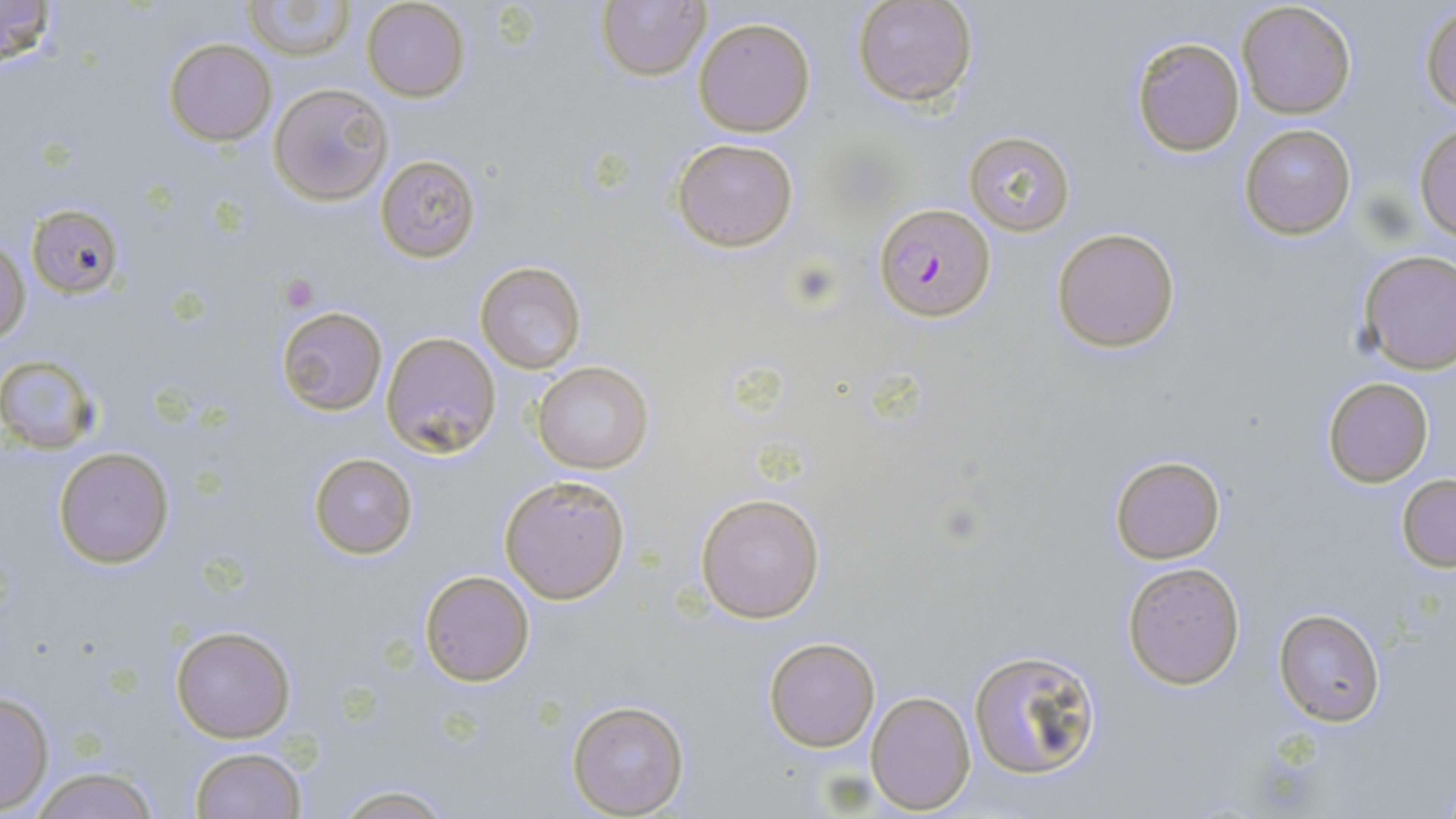
slide-level diagnosis = Plasmodium falciparum
modality = light microscopy
stain = May-Grünwald-Giemsa
image size = 1456×819 pixels
magnification = 1000x
uninfected red blood cell locations = approximate bounding boxes as named x1/y1/x2/y2 corners in pixels: (x1=0, y1=0, x2=57, y2=68), (x1=245, y1=0, x2=354, y2=61), (x1=597, y1=0, x2=711, y2=82), (x1=852, y1=0, x2=977, y2=109), (x1=362, y1=1, x2=468, y2=102), (x1=1237, y1=2, x2=1356, y2=118), (x1=1420, y1=5, x2=1455, y2=116), (x1=692, y1=17, x2=816, y2=137), (x1=1129, y1=35, x2=1246, y2=156), (x1=164, y1=38, x2=275, y2=147), (x1=270, y1=82, x2=392, y2=206), (x1=1239, y1=123, x2=1357, y2=240), (x1=1414, y1=123, x2=1456, y2=241), (x1=963, y1=130, x2=1076, y2=237), (x1=671, y1=137, x2=801, y2=253), (x1=374, y1=153, x2=481, y2=263), (x1=26, y1=201, x2=126, y2=298), (x1=1051, y1=226, x2=1182, y2=353), (x1=1, y1=235, x2=29, y2=345), (x1=1356, y1=248, x2=1456, y2=375), (x1=475, y1=260, x2=588, y2=374), (x1=276, y1=306, x2=387, y2=416), (x1=380, y1=332, x2=502, y2=457), (x1=0, y1=356, x2=103, y2=453), (x1=532, y1=360, x2=654, y2=476), (x1=1323, y1=376, x2=1434, y2=487), (x1=54, y1=447, x2=173, y2=568), (x1=308, y1=452, x2=417, y2=559), (x1=1110, y1=455, x2=1226, y2=565), (x1=1396, y1=473, x2=1456, y2=571), (x1=499, y1=475, x2=631, y2=603), (x1=695, y1=492, x2=825, y2=623), (x1=1121, y1=562, x2=1247, y2=689), (x1=419, y1=569, x2=536, y2=687), (x1=1274, y1=607, x2=1386, y2=725), (x1=171, y1=625, x2=296, y2=743), (x1=763, y1=638, x2=881, y2=752), (x1=967, y1=648, x2=1103, y2=784), (x1=0, y1=689, x2=55, y2=815), (x1=866, y1=690, x2=975, y2=811), (x1=565, y1=698, x2=691, y2=817), (x1=189, y1=745, x2=307, y2=818), (x1=25, y1=765, x2=161, y2=819), (x1=323, y1=783, x2=459, y2=818)
platelet locations = approximate bounding boxes as named x1/y1/x2/y2 corners in pixels: (x1=277, y1=274, x2=319, y2=312)
preparation = thin blood film
field of view = single
Plasmodium falciparum-infected red blood cell locations = approximate bounding boxes as named x1/y1/x2/y2 corners in pixels: (x1=875, y1=201, x2=996, y2=321)